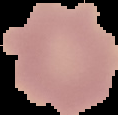
Summary:
  - Image size: 118×115 pixels
  - Malaria status: uninfected
  - Preparation: thin blood film
  - Image type: cell region segmented out of the field of view; surrounding area masked to black